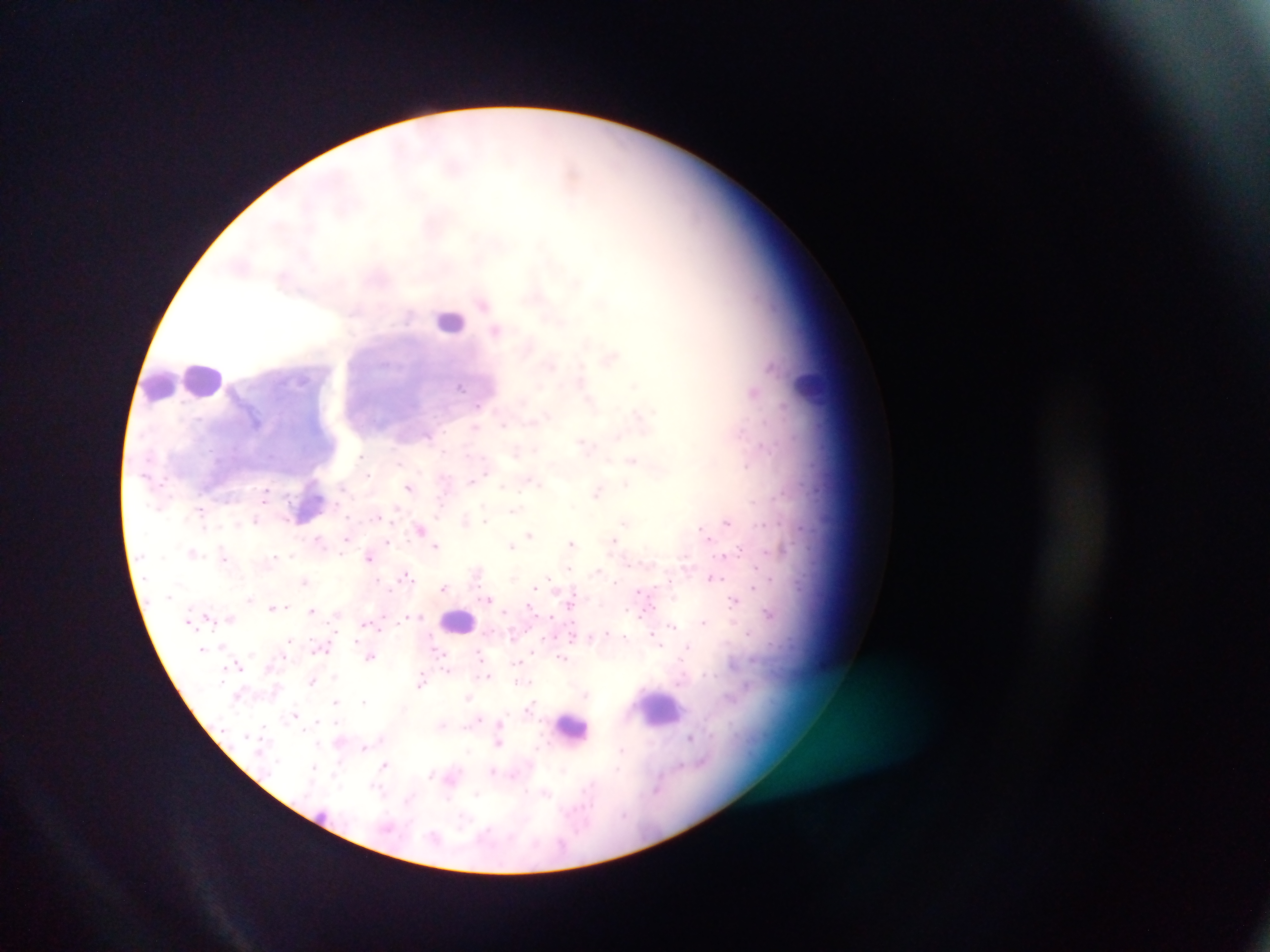

{
  "image_size": "1270×952 pixels",
  "malaria_parasite_locations": "approximate centers as x y in pixels: 482 302; 496 329; 634 385; 460 386; 754 392; 478 405; 547 415; 199 419; 504 425; 475 428; 427 435; 618 437; 584 443; 761 444; 535 448; 443 451; 516 452; 359 455; 632 460; 399 463; 746 466; 485 470; 368 474; 481 475; 471 480; 531 480; 626 483; 342 486; 502 486; 409 488; 267 492; 597 492; 572 505; 200 509; 514 511; 379 517; 465 520; 256 521; 484 521; 727 522; 625 523; 420 529; 703 531; 530 534; 707 537; 318 539; 346 539; 614 540; 388 542; 571 543; 436 546; 511 546; 738 550; 192 552; 342 554; 291 555; 223 556; 274 557; 368 557; 755 567; 570 569; 596 570; 476 574; 406 575; 713 577; 548 578; 304 581; 669 582; 444 587; 534 587; 638 592; 573 595; 250 599; 489 599; 734 600; 272 606; 285 606; 529 607; 625 609; 311 610; 505 612; 767 613; 207 615; 410 615; 418 615; 551 616; 230 618; 704 621; 672 625; 607 632; 572 634; 590 636; 626 638; 288 640; 356 640; 660 646; 687 646; 202 649; 438 652; 534 652; 480 653; 284 656; 371 656; 562 658; 238 663; 517 664; 447 670; 489 675; 313 681; 520 681; 526 681; 420 682; 586 694; 468 698; 334 701; 364 701; 531 706; 295 715; 477 719; 335 721; 500 722; 442 726; 263 728; 690 737; 380 738; 499 743; 318 744; 364 748; 537 748; 621 749; 468 751; 340 762; 384 765; 681 765; 315 768; 563 769; 492 771; 430 774; 513 775; 590 785; 377 787; 656 789; 546 793; 477 794; 447 798; 409 799; 463 819",
  "country": "Ghana",
  "field_of_view": "single",
  "leukocyte_locations": "approximate centers as x y in pixels: 450 320; 205 380; 158 384; 811 389; 459 620; 664 709; 566 725",
  "capture": "mobile-phone photograph through a microscope",
  "preparation": "thick blood smear"
}